Assess for Plasmodium parasites.
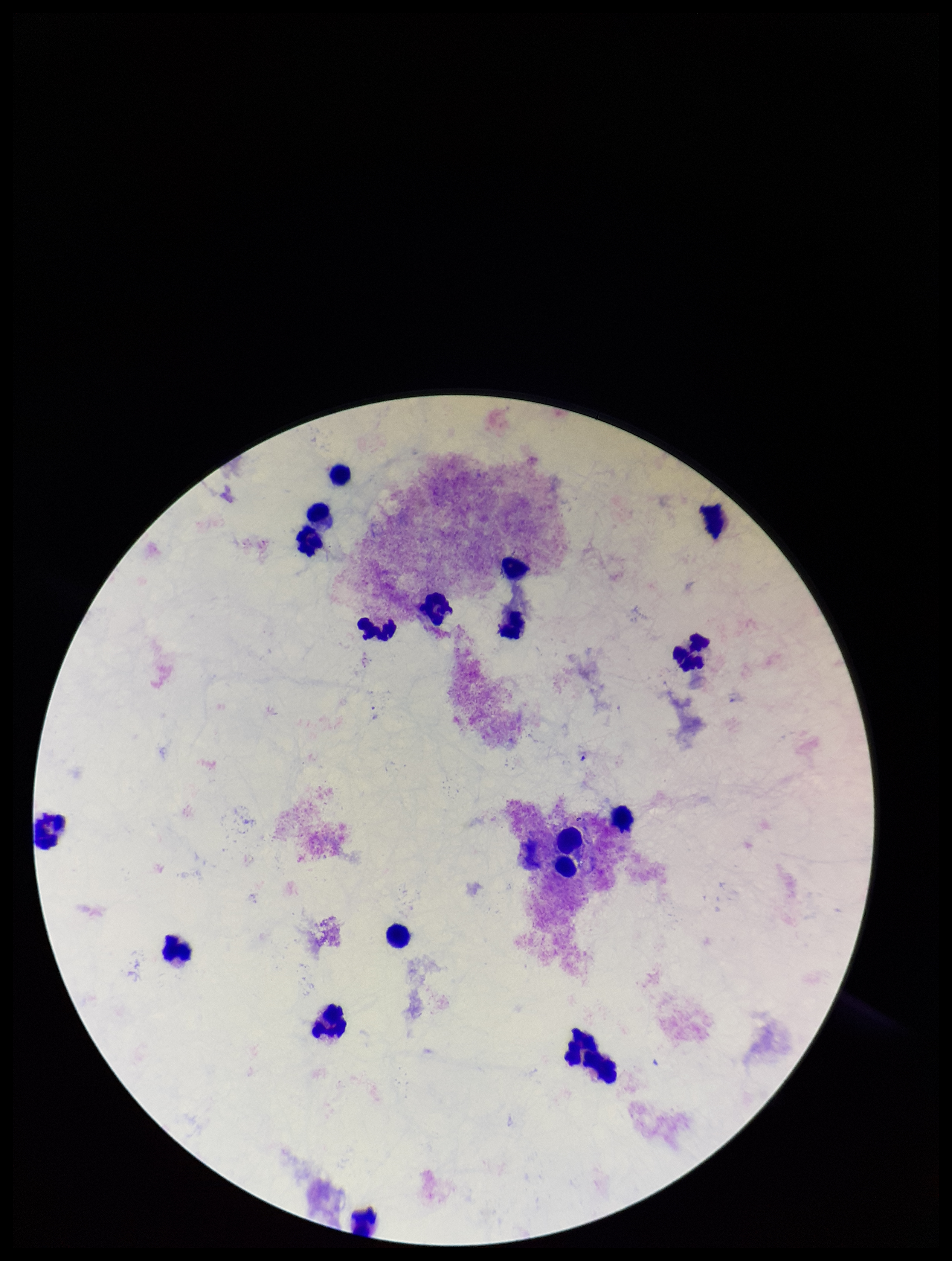
None identified.

patient malaria status = negative
field of view = single
stain = Giemsa
preparation = thick
capture = smartphone photograph through the microscope eyepiece
image size = 952×1261 pixels
leukocyte count = 18
parasite count = 0